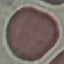

malaria_status: uninfected
stain: Giemsa
image_type: cell patch, automatically extracted from a larger field of view and resized to 64 × 64 pixels
preparation: thin smear
capture: smartphone camera at the microscope eyepiece